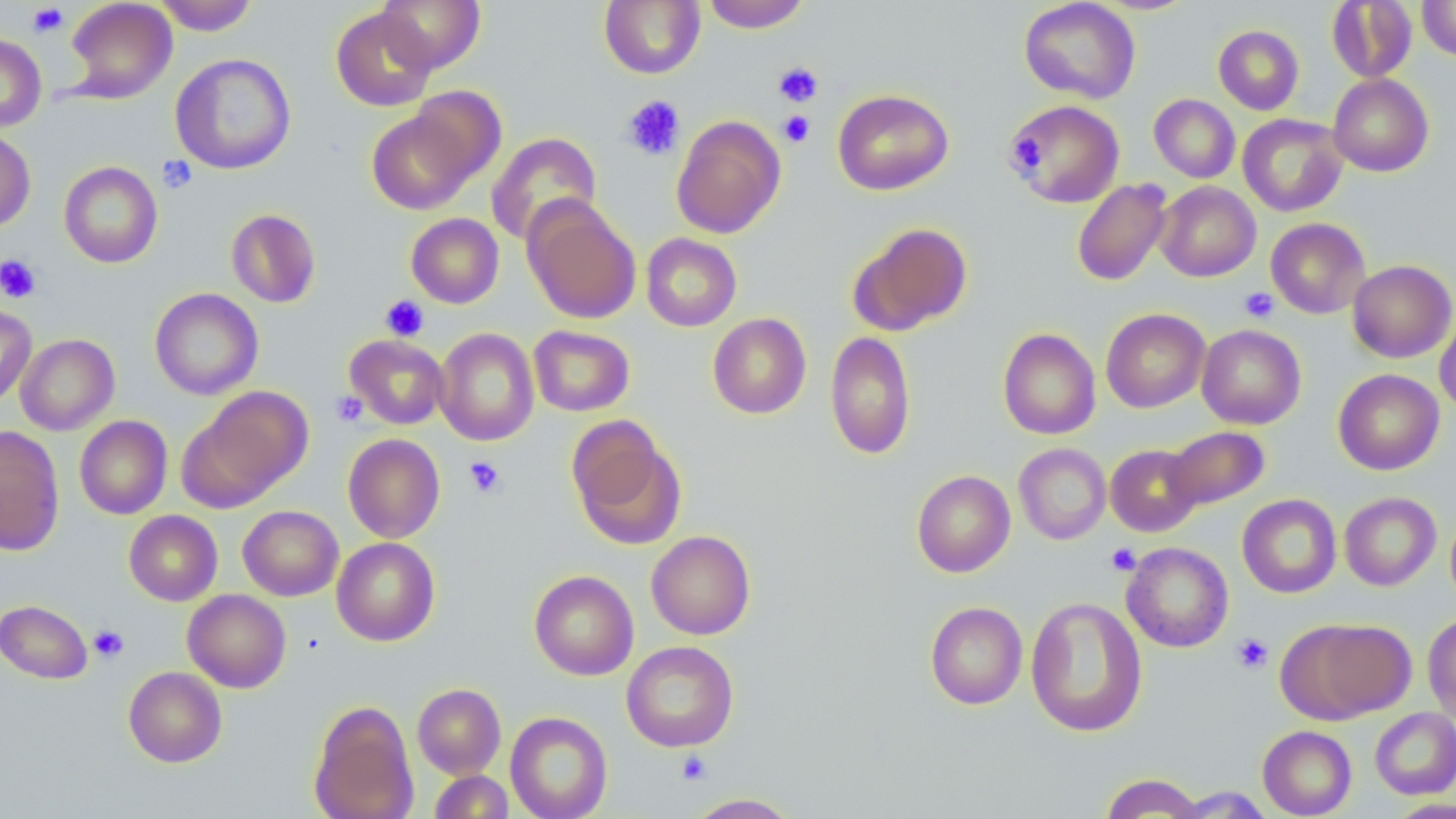

Summary:
  - Coordinate format: approximate bounding boxes as (x1,y1)-(x2,y2) corner pairs in pixels
  - Uninfected red blood cell locations: (64,0)-(178,103), (155,0)-(260,35), (376,0)-(485,73), (701,0)-(811,32), (1019,0)-(1140,104), (1417,0)-(1456,61), (599,1)-(705,79), (1326,1)-(1418,83), (330,6)-(437,112), (1213,25)-(1304,115), (0,33)-(47,132), (170,53)-(296,174), (1328,73)-(1433,176), (408,86)-(506,185), (832,88)-(954,195), (1149,94)-(1240,183), (1006,99)-(1125,207), (366,109)-(476,215), (671,114)-(786,239), (1238,114)-(1348,217), (0,128)-(35,231), (486,132)-(602,245), (59,161)-(163,268), (1072,178)-(1172,286), (1155,181)-(1261,282), (523,198)-(641,325), (226,208)-(321,308), (406,213)-(504,308), (1266,218)-(1370,318), (849,221)-(972,335), (641,233)-(742,332), (1347,260)-(1455,363), (150,288)-(263,400), (0,304)-(36,407), (1101,308)-(1210,413), (1435,310)-(1456,415), (707,313)-(811,419), (1196,324)-(1306,429), (528,325)-(635,417), (434,327)-(539,446), (998,328)-(1101,440), (824,331)-(916,459), (15,334)-(119,435), (344,335)-(449,429), (1333,369)-(1445,475), (194,386)-(312,502), (75,415)-(172,519), (568,420)-(685,549), (1163,425)-(1271,512), (0,426)-(65,555), (343,433)-(445,543), (1013,443)-(1111,545), (1106,444)-(1203,536), (911,470)-(1015,577), (1339,491)-(1441,591), (1237,494)-(1341,598), (238,505)-(343,600), (124,510)-(222,606), (1445,510)-(1456,609), (646,530)-(756,640), (331,537)-(440,646), (1122,542)-(1233,652), (529,570)-(639,680), (182,589)-(291,693), (1025,597)-(1147,737), (0,600)-(92,684), (925,601)-(1027,709), (1422,614)-(1456,723), (1287,618)-(1416,720), (622,641)-(739,752), (123,666)-(227,767), (412,683)-(506,778), (308,700)-(419,819), (1370,707)-(1456,799), (505,711)-(613,819), (1258,725)-(1357,818), (429,770)-(514,818), (1099,773)-(1206,818), (1169,786)-(1275,817), (685,793)-(802,818), (1384,798)-(1456,818)
  - Platelet locations: (27,4)-(68,36), (773,62)-(823,106), (621,95)-(685,161), (779,111)-(814,147), (1010,135)-(1047,173), (157,155)-(198,193), (0,254)-(41,303), (1239,287)-(1278,322), (381,295)-(429,342), (330,391)-(368,428), (464,456)-(506,498), (1105,543)-(1141,575), (89,625)-(129,662), (1232,634)-(1273,674), (677,750)-(712,784)
  - Slide-level diagnosis: no evidence of blood parasites
  - Field of view: one of a larger specimen
  - Stain: May-Grünwald-Giemsa
  - Modality: optical microscopy
  - Preparation: thin blood smear
  - Magnification: 1000x
  - Image size: 1456×819 pixels